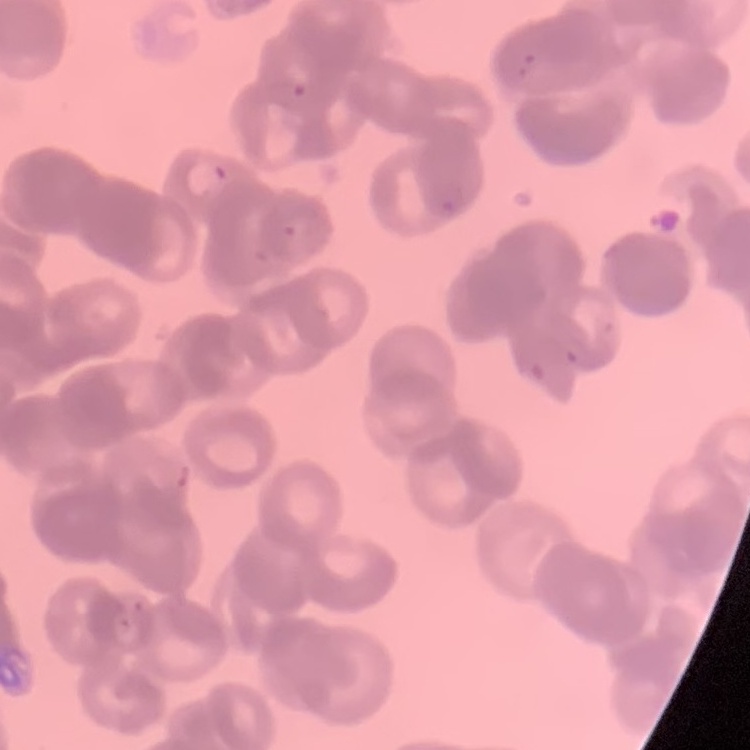
Summary:
  - Erythrocyte morphology: rouleaux formation
  - Image type: one tile cut from a larger photomicrograph
  - Stain: Field's or Giemsa
  - Preparation: thin blood film